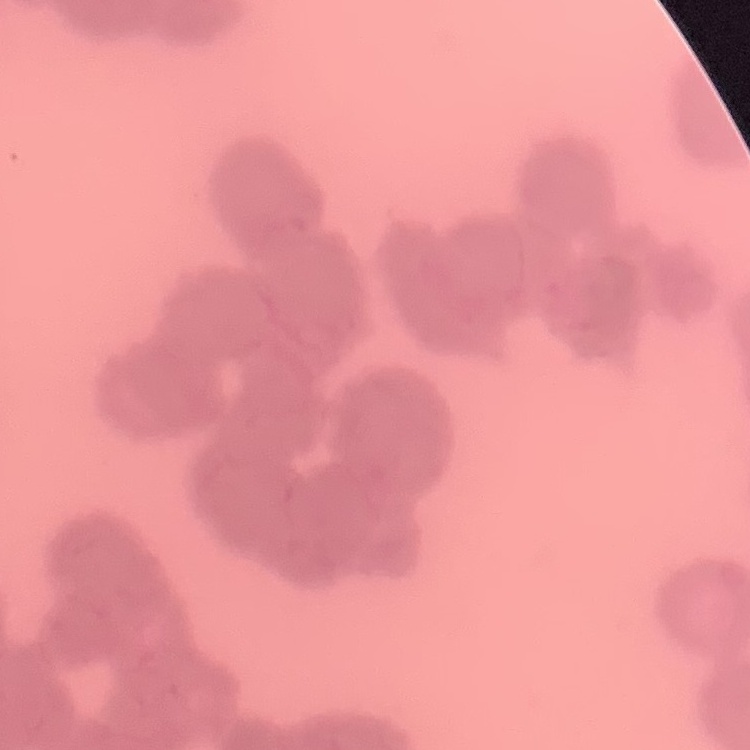

The red blood cells exhibit rouleaux formation. Thin peripheral smear. One tile cut from a larger photomicrograph. Stained with either Field's or Giemsa.